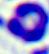

Captured at 400x magnification. Micrograph. A white blood cell is seen.